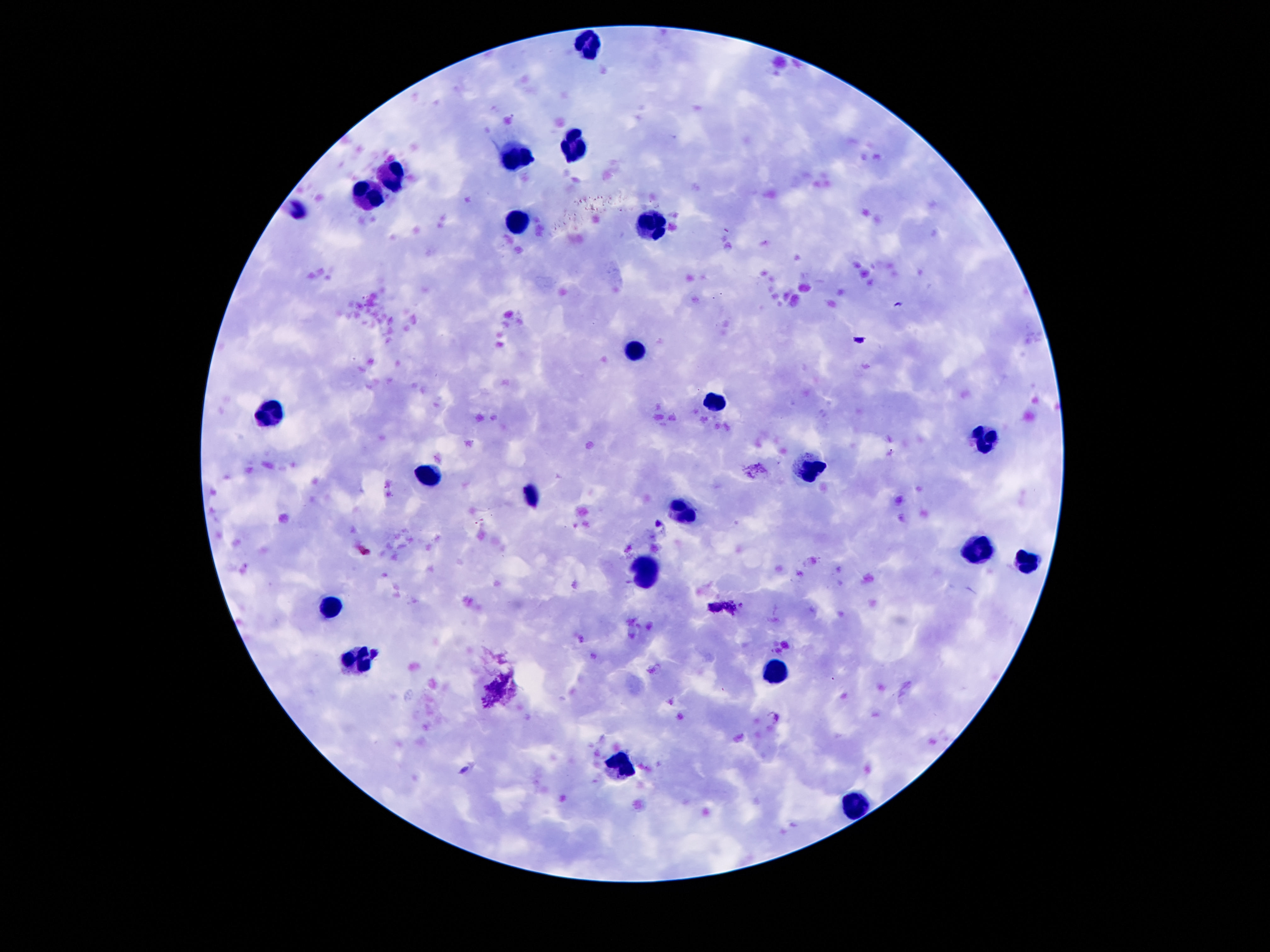

{
  "leukocyte_locations": "approximate centers as (x, y) in pixels: (588, 42), (573, 148), (517, 154), (388, 174), (366, 202), (517, 221), (650, 225), (635, 350), (713, 402), (274, 415), (984, 436), (812, 471), (426, 477), (530, 499), (683, 512), (978, 548), (1030, 563), (644, 574), (336, 604), (360, 658), (775, 671), (616, 763), (855, 802)",
  "image_size": "1270×952 pixels",
  "patient_malaria_status": "uninfected",
  "field_of_view": "single",
  "magnification": "100x",
  "preparation": "thick blood film",
  "stain": "Giemsa",
  "capture": "smartphone camera through the microscope eyepiece"
}